Name the parasite shown.
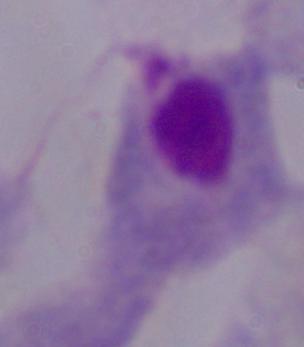
A trichomonad.

Photomicrograph. 1000x magnification.